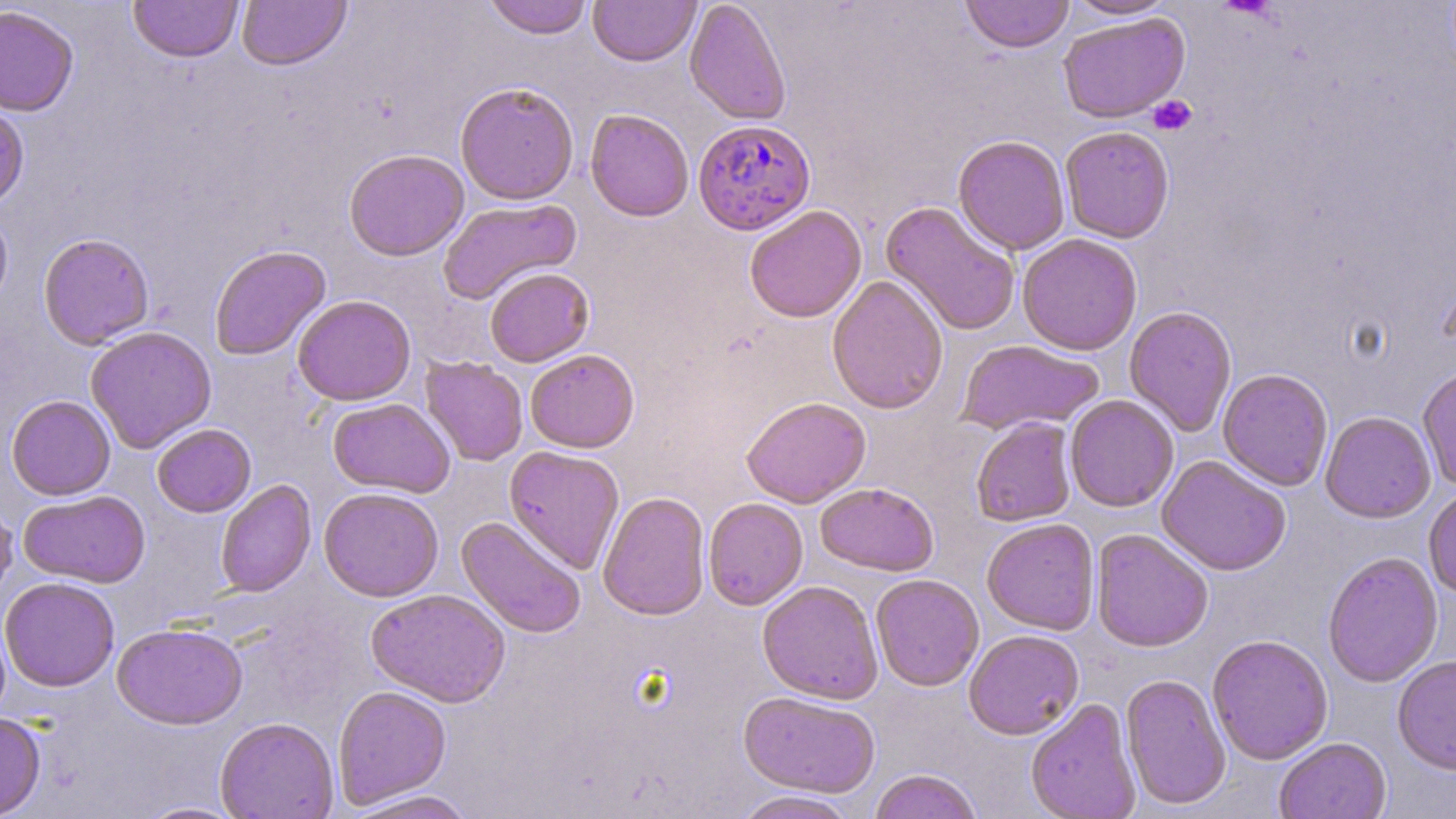
slide-level diagnosis = Plasmodium falciparum
stain = May-Grünwald-Giemsa
magnification = 1000x
platelet locations = approximate bounding boxes as (x1, y1, x2, y2) in pixels: (1147, 95, 1197, 136)
image size = 1456×819 pixels
field of view = one of a larger specimen
uninfected red blood cell locations = approximate bounding boxes as (x1, y1, x2, y2) in pixels: (128, 0, 244, 63), (237, 0, 352, 72), (483, 0, 593, 39), (588, 0, 701, 67), (684, 0, 792, 125), (960, 0, 1074, 53), (1064, 0, 1177, 20), (0, 5, 79, 116), (1057, 12, 1190, 124), (455, 81, 579, 205), (0, 104, 29, 210), (585, 109, 694, 222), (1060, 125, 1175, 243), (953, 134, 1070, 255), (344, 148, 469, 261), (437, 198, 583, 305), (880, 201, 1021, 336), (0, 205, 13, 313), (744, 205, 867, 323), (38, 233, 155, 349), (1017, 233, 1143, 356), (209, 245, 331, 361), (484, 267, 594, 367), (826, 275, 949, 414), (293, 295, 416, 406), (1123, 305, 1237, 437), (85, 326, 217, 454), (956, 339, 1105, 436), (524, 349, 639, 453), (420, 357, 528, 466), (1417, 366, 1456, 490), (1218, 368, 1334, 491), (6, 395, 116, 500), (1064, 395, 1179, 513), (741, 396, 871, 508), (328, 398, 455, 498), (1320, 411, 1436, 523), (971, 417, 1077, 527), (152, 423, 256, 517), (503, 445, 625, 574), (1156, 455, 1291, 576), (215, 479, 316, 597), (815, 483, 939, 576), (1423, 485, 1456, 599), (318, 486, 444, 602), (18, 490, 151, 588), (598, 491, 710, 620), (0, 495, 18, 608), (703, 497, 809, 610), (456, 516, 587, 638), (981, 517, 1100, 635), (1091, 529, 1214, 652), (1322, 551, 1443, 687), (870, 574, 984, 691), (1, 576, 120, 692), (757, 580, 883, 704), (366, 588, 510, 707), (112, 622, 248, 729), (963, 629, 1084, 740), (1207, 634, 1333, 765), (1392, 654, 1456, 775), (1120, 673, 1231, 811), (333, 685, 451, 808), (738, 690, 881, 797), (1025, 697, 1141, 819), (0, 712, 46, 818), (215, 717, 339, 819), (1274, 738, 1392, 819), (868, 769, 982, 819), (344, 789, 478, 818), (731, 790, 861, 818), (135, 801, 249, 819)
Plasmodium falciparum-infected red blood cell locations = approximate bounding boxes as (x1, y1, x2, y2) in pixels: (693, 119, 816, 236)
modality = optical microscopy
preparation = thin blood film